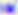

modality = micrograph
identification = Toxoplasma gondii
magnification = 400x